Report the malaria status of this cell.
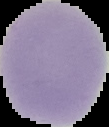
Uninfected.

preparation: thin blood film
image_type: segmented cell region on a black background
image_size: 109×127 pixels